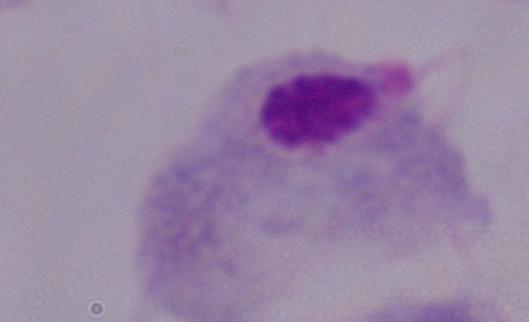
A trichomonad is seen. Captured at 1000x magnification. Micrograph.